Comment on the morphology of the erythrocytes.
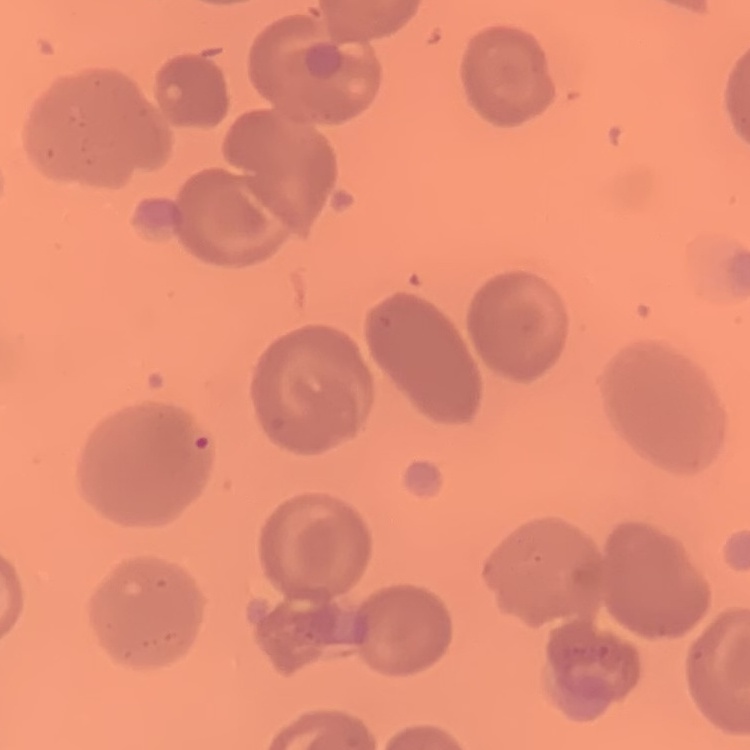

They show no rouleaux formation.

Summary:
  - Image type: one tile cut from a larger photomicrograph
  - Stain: Field's or Giemsa
  - Preparation: thin peripheral smear